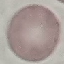
Malaria status: uninfected. Thin smear of blood. Acquired by smartphone through the microscope eyepiece. Cell patch, automatically extracted from a larger field of view and resized to 64 × 64 pixels. Giemsa-stained preparation.